Assess this cell for malaria.
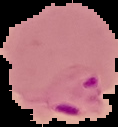
Parasitized.

Summary:
  - Preparation: thin blood smear
  - Image size: 118×127 pixels
  - Image type: segmented cell region with the area outside set to black